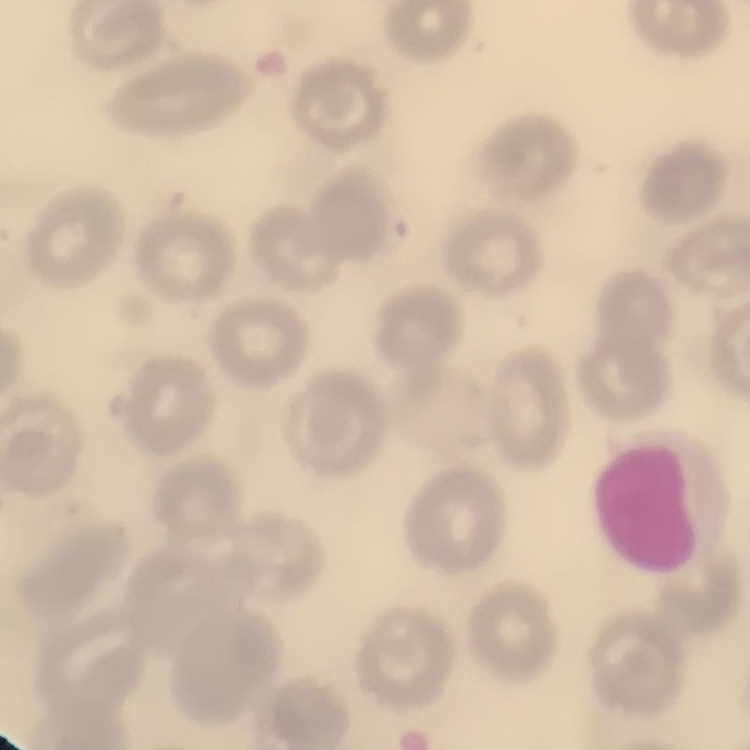

Summary:
  - Red blood cell morphology: no rouleaux formation
  - Stain: Field's or Giemsa
  - Image type: one tile cut from a larger photomicrograph
  - Preparation: thin peripheral smear